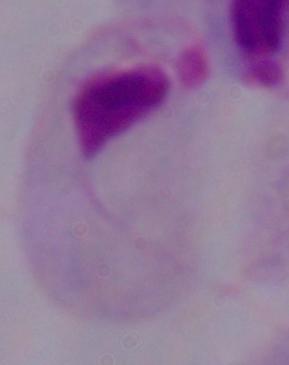

Micrograph. Captured at 1000x magnification. A trichomonad is seen.